Locate every blood parasite and identify its species.
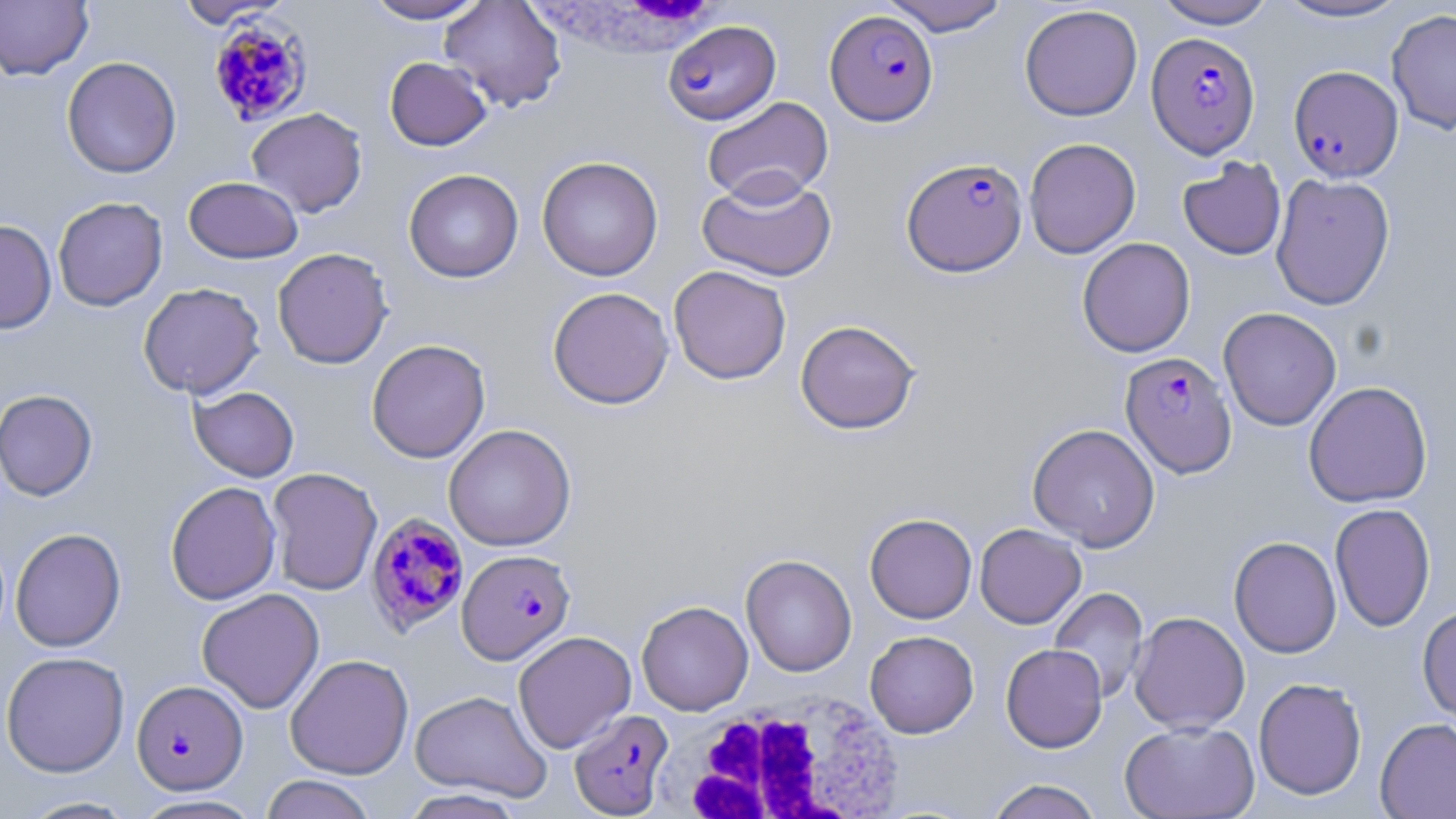

Approximate bounding boxes as named x1/y1/x2/y2 corners in pixels.
Plasmodium falciparum-infected red blood cells: (x1=825, y1=9, x2=939, y2=125), (x1=208, y1=17, x2=314, y2=127), (x1=663, y1=20, x2=781, y2=125), (x1=1145, y1=32, x2=1260, y2=158), (x1=1288, y1=65, x2=1403, y2=182), (x1=901, y1=156, x2=1028, y2=277), (x1=1120, y1=351, x2=1237, y2=477), (x1=365, y1=512, x2=470, y2=637), (x1=457, y1=548, x2=575, y2=664), (x1=132, y1=680, x2=248, y2=794), (x1=569, y1=709, x2=674, y2=817).
No Plasmodium ovale, Plasmodium malariae, Plasmodium vivax, Babesia divergens, or Trypanosoma brucei observed.

White blood cell locations: (x1=523, y1=0, x2=740, y2=58), (x1=664, y1=688, x2=909, y2=819). Uninfected red blood cell locations: (x1=173, y1=0, x2=293, y2=28), (x1=362, y1=0, x2=489, y2=24), (x1=439, y1=0, x2=567, y2=112), (x1=878, y1=0, x2=1012, y2=36), (x1=1152, y1=0, x2=1278, y2=29), (x1=1271, y1=0, x2=1412, y2=23), (x1=0, y1=1, x2=93, y2=81), (x1=1019, y1=4, x2=1143, y2=121), (x1=1387, y1=9, x2=1456, y2=135), (x1=61, y1=56, x2=182, y2=178), (x1=384, y1=56, x2=492, y2=151), (x1=702, y1=96, x2=834, y2=206), (x1=246, y1=107, x2=367, y2=217), (x1=1024, y1=137, x2=1141, y2=259), (x1=537, y1=155, x2=664, y2=281), (x1=1177, y1=157, x2=1287, y2=260), (x1=403, y1=169, x2=524, y2=283), (x1=696, y1=171, x2=837, y2=282), (x1=1270, y1=173, x2=1395, y2=310), (x1=183, y1=176, x2=304, y2=263), (x1=52, y1=196, x2=168, y2=311), (x1=0, y1=220, x2=57, y2=334), (x1=1077, y1=237, x2=1196, y2=357), (x1=272, y1=247, x2=394, y2=369), (x1=668, y1=265, x2=792, y2=385), (x1=138, y1=282, x2=265, y2=398), (x1=547, y1=286, x2=675, y2=409), (x1=1218, y1=307, x2=1342, y2=431), (x1=795, y1=319, x2=921, y2=434), (x1=366, y1=339, x2=491, y2=463), (x1=1303, y1=381, x2=1433, y2=508), (x1=189, y1=386, x2=300, y2=482), (x1=0, y1=389, x2=98, y2=501), (x1=1027, y1=423, x2=1160, y2=551), (x1=443, y1=424, x2=576, y2=551), (x1=266, y1=467, x2=382, y2=595), (x1=165, y1=481, x2=282, y2=605), (x1=1330, y1=503, x2=1436, y2=632), (x1=865, y1=513, x2=977, y2=624), (x1=974, y1=523, x2=1086, y2=628), (x1=10, y1=528, x2=126, y2=652), (x1=1228, y1=536, x2=1342, y2=658), (x1=740, y1=554, x2=857, y2=677), (x1=1048, y1=587, x2=1149, y2=704), (x1=196, y1=588, x2=325, y2=714), (x1=636, y1=600, x2=753, y2=715), (x1=1417, y1=603, x2=1456, y2=726), (x1=1129, y1=611, x2=1250, y2=734), (x1=865, y1=630, x2=979, y2=738), (x1=513, y1=631, x2=636, y2=753), (x1=1000, y1=643, x2=1108, y2=753), (x1=1, y1=651, x2=130, y2=777), (x1=285, y1=654, x2=414, y2=779), (x1=1253, y1=677, x2=1367, y2=800), (x1=409, y1=690, x2=552, y2=801), (x1=1375, y1=717, x2=1456, y2=819), (x1=1119, y1=720, x2=1260, y2=818), (x1=259, y1=774, x2=378, y2=819), (x1=983, y1=779, x2=1105, y2=819), (x1=399, y1=788, x2=527, y2=818), (x1=131, y1=795, x2=264, y2=818), (x1=17, y1=796, x2=138, y2=818). Slide-level diagnosis: Plasmodium falciparum. Thin blood smear. Image is 1456×819 pixels. One field of a larger specimen. Captured at 1000x magnification. May-Grünwald-Giemsa-stained preparation. Optical microscopy.